Locate every malaria parasite and every leukocyte.
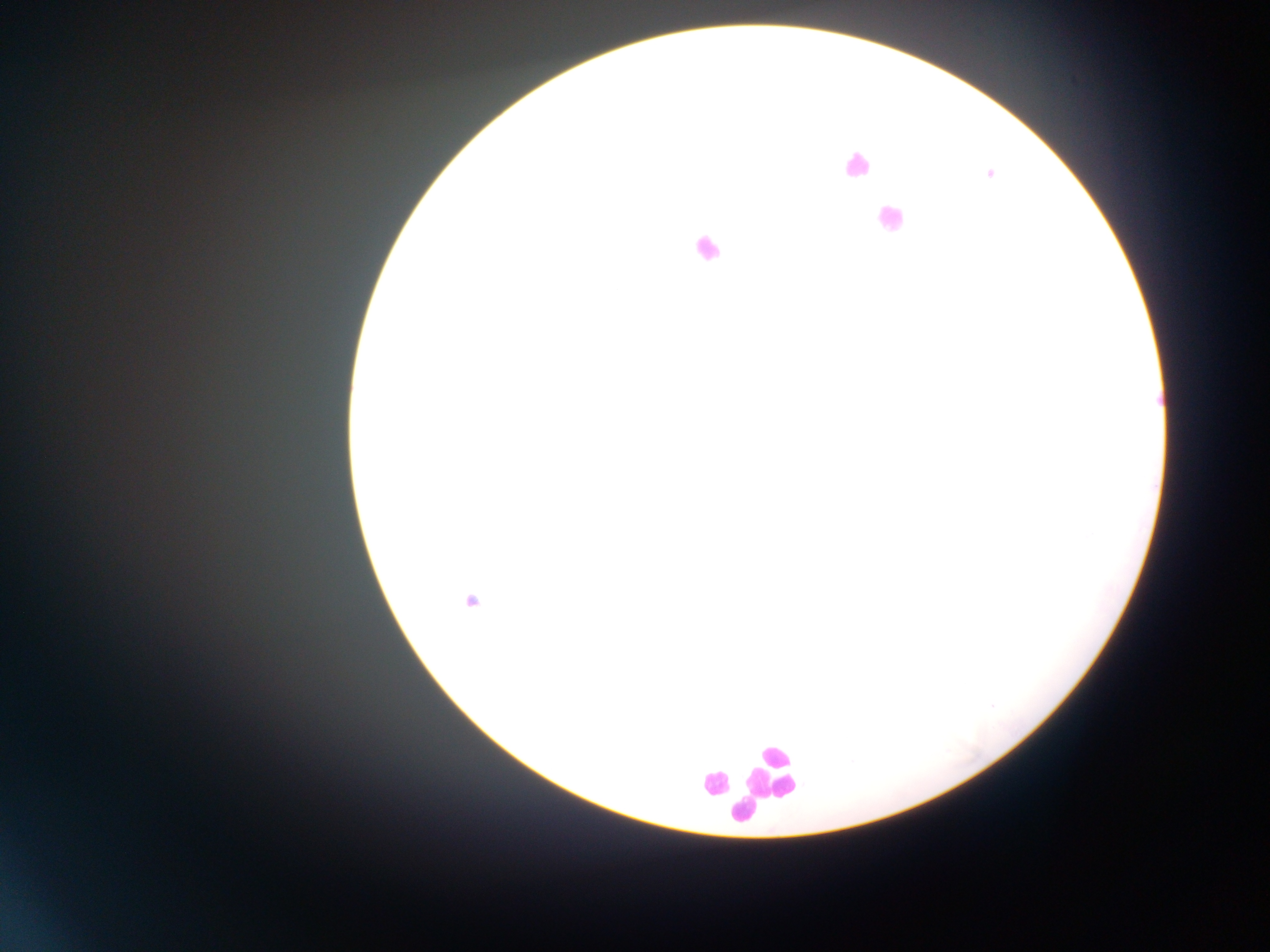
Approximate centers as {x, y} in pixels.
Malaria parasites: {989, 175}, {471, 602}, {992, 706}.
Leukocytes: {856, 164}, {888, 219}, {705, 248}, {771, 770}, {713, 784}, {744, 812}.

{
  "preparation": "thick blood smear",
  "image_size": "1270×952 pixels",
  "capture": "mobile-phone photograph through a microscope",
  "country": "Ghana",
  "field_of_view": "single"
}